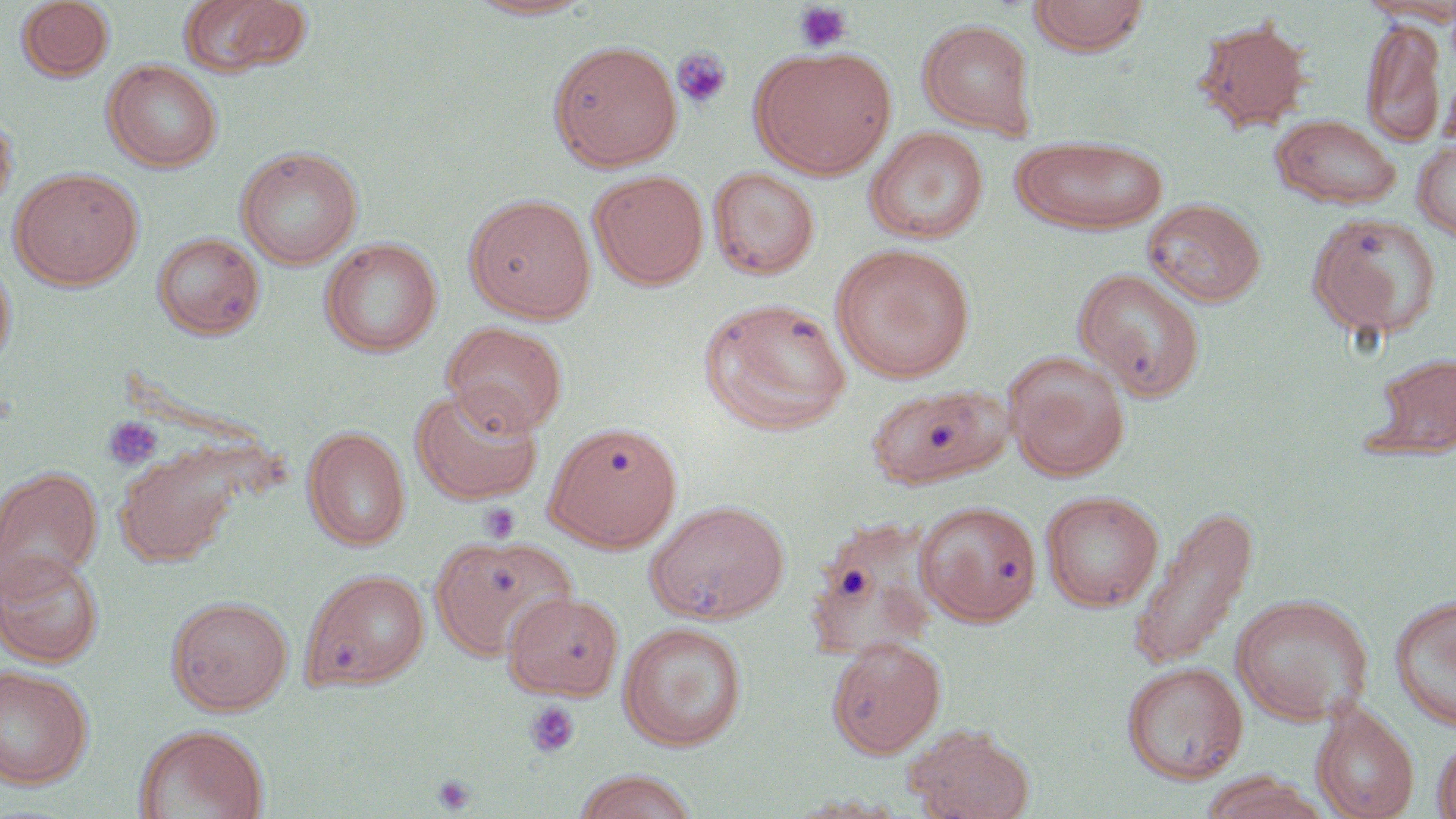
slide-level diagnosis = no evidence of blood parasites
uninfected red blood cell locations = approximate bounding boxes as [x1, y1, x2, y2] in pixels: [15, 0, 114, 82], [176, 0, 312, 78], [465, 0, 598, 20], [1028, 0, 1150, 56], [1357, 0, 1456, 25], [1192, 16, 1312, 134], [1361, 17, 1445, 147], [916, 19, 1039, 139], [547, 39, 683, 171], [750, 46, 896, 179], [103, 59, 222, 172], [0, 107, 17, 217], [1269, 114, 1403, 209], [865, 127, 989, 245], [1011, 135, 1169, 235], [1412, 140, 1456, 241], [236, 146, 363, 269], [9, 167, 143, 289], [709, 167, 820, 280], [588, 170, 709, 290], [464, 193, 596, 323], [1142, 198, 1267, 307], [1306, 212, 1442, 342], [153, 232, 265, 340], [321, 238, 441, 357], [831, 244, 976, 383], [0, 253, 16, 375], [1074, 267, 1207, 401], [699, 297, 852, 435], [442, 321, 568, 437], [1365, 351, 1456, 460], [1004, 352, 1129, 480], [867, 383, 1012, 490], [410, 387, 543, 505], [545, 420, 683, 550], [303, 425, 411, 551], [115, 448, 240, 567], [0, 467, 103, 594], [1040, 490, 1164, 612], [644, 499, 790, 623], [915, 500, 1042, 626], [1127, 503, 1259, 672], [803, 518, 943, 663], [430, 535, 576, 660], [0, 549, 104, 667], [300, 569, 430, 691], [502, 590, 625, 701], [1231, 593, 1374, 726], [166, 594, 293, 715], [1389, 594, 1456, 731], [618, 621, 749, 750], [826, 636, 946, 758], [1122, 661, 1249, 783], [0, 664, 94, 788], [1311, 701, 1419, 819], [134, 724, 269, 819], [903, 725, 1035, 819], [1431, 733, 1456, 818], [571, 770, 701, 819], [1200, 772, 1330, 819], [785, 793, 910, 817]
platelet locations = approximate bounding boxes as [x1, y1, x2, y2] in pixels: [792, 2, 853, 54], [671, 47, 732, 110], [102, 415, 164, 471], [479, 502, 521, 542], [525, 700, 581, 758], [432, 773, 477, 814]
preparation = thin blood film
modality = light microscopy
stain = May-Grünwald-Giemsa
magnification = 1000x
field of view = one of a larger specimen
image size = 1456×819 pixels